Locate every Plasmodium falciparum-infected red blood cell.
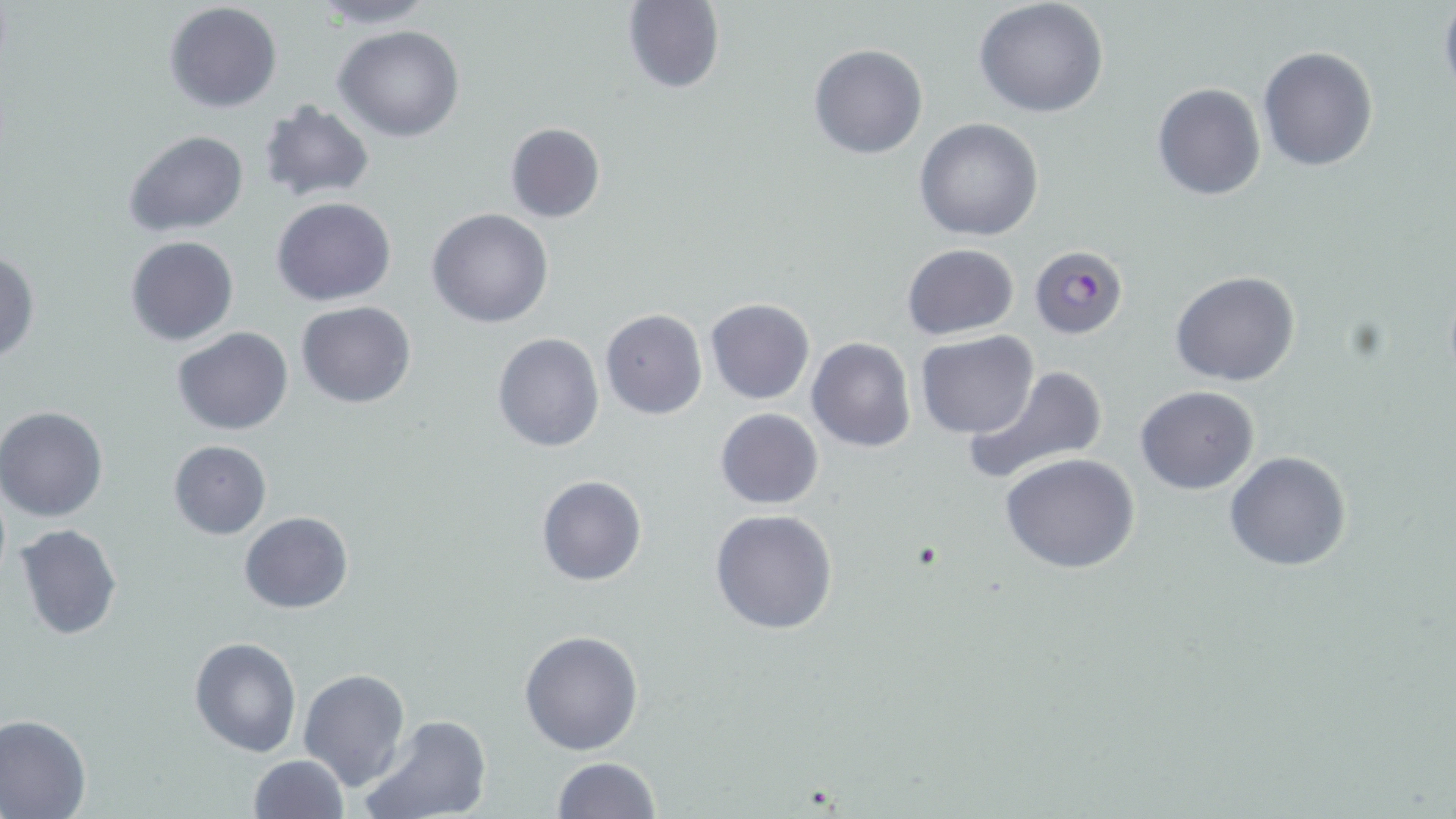

Approximate bounding boxes as (x1, y1, x2, y2) in pixels.
Plasmodium falciparum-infected red blood cells: (1029, 246, 1126, 339).

{
  "slide_level_diagnosis": "Plasmodium falciparum",
  "image_size": "1456×819 pixels",
  "stain": "May-Grünwald-Giemsa",
  "uninfected_red_blood_cell_locations": "approximate bounding boxes as (x1, y1, x2, y2) in pixels: (305, 0, 441, 29), (973, 0, 1111, 119), (620, 1, 725, 93), (164, 2, 283, 115), (1438, 2, 1456, 102), (334, 25, 465, 142), (808, 44, 928, 160), (1257, 46, 1379, 171), (273, 71, 432, 194), (1152, 84, 1265, 200), (257, 102, 374, 201), (914, 119, 1044, 241), (504, 121, 605, 223), (123, 129, 249, 239), (272, 197, 396, 306), (427, 207, 555, 328), (125, 236, 238, 346), (901, 244, 1019, 340), (0, 251, 40, 365), (1170, 272, 1299, 388), (705, 298, 815, 405), (297, 301, 416, 408), (599, 310, 707, 420), (171, 325, 293, 435), (491, 331, 605, 452), (914, 331, 1039, 440), (806, 337, 916, 454), (962, 366, 1107, 486), (1134, 386, 1258, 496), (0, 405, 109, 523), (715, 407, 824, 510), (168, 440, 271, 539), (1225, 451, 1351, 572), (998, 454, 1141, 573), (536, 476, 647, 587), (710, 509, 838, 634), (239, 510, 354, 614), (14, 522, 122, 641), (518, 629, 644, 756), (190, 635, 301, 757), (298, 668, 411, 791), (0, 714, 93, 818), (360, 715, 492, 819), (247, 755, 348, 818), (550, 757, 660, 818)",
  "preparation": "thin blood film",
  "modality": "light microscopy",
  "magnification": "1000x",
  "field_of_view": "one of a larger specimen"
}